Comment on the morphology of the red blood cells.
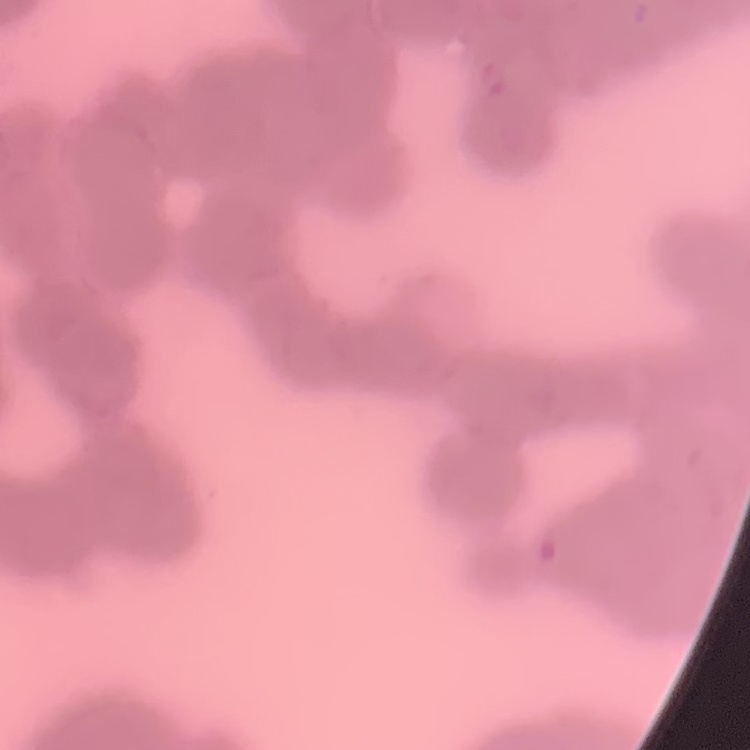

They show rouleaux formation.

Summary:
  - Stain: Field's or Giemsa
  - Preparation: thin blood smear
  - Image type: square crop of a larger photomicrograph